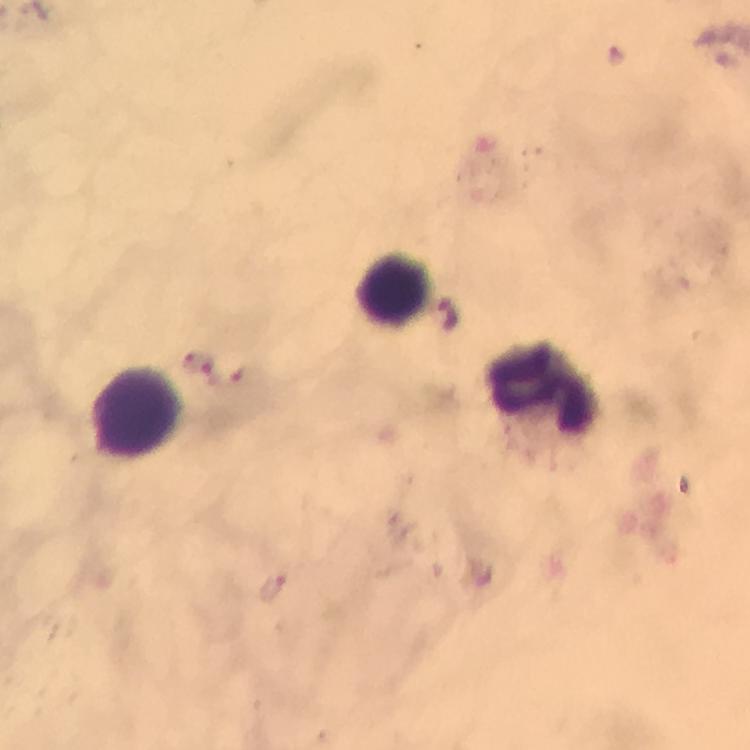
{
  "image_size": "750×750 pixels",
  "preparation": "thick smear",
  "leukocyte_locations": "approximate centers as {x, y} in pixels: {394, 286}, {544, 387}, {136, 412}",
  "capture": "smartphone photograph through a microscope",
  "stain": "Giemsa",
  "malaria_parasite_locations": "approximate centers as {x, y} in pixels: {445, 311}, {215, 372}, {273, 586}",
  "cropped_from": "one field of view",
  "context": "from a diagnostic examination for malaria",
  "magnification": "100x",
  "immersion_oil": "used"
}